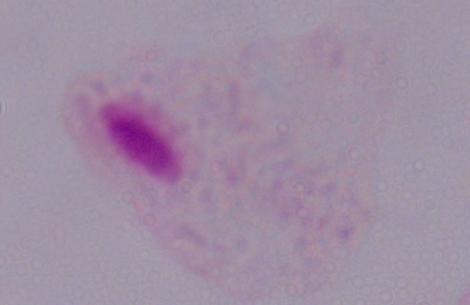
identification: trichomonad
modality: micrograph
magnification: 1000x